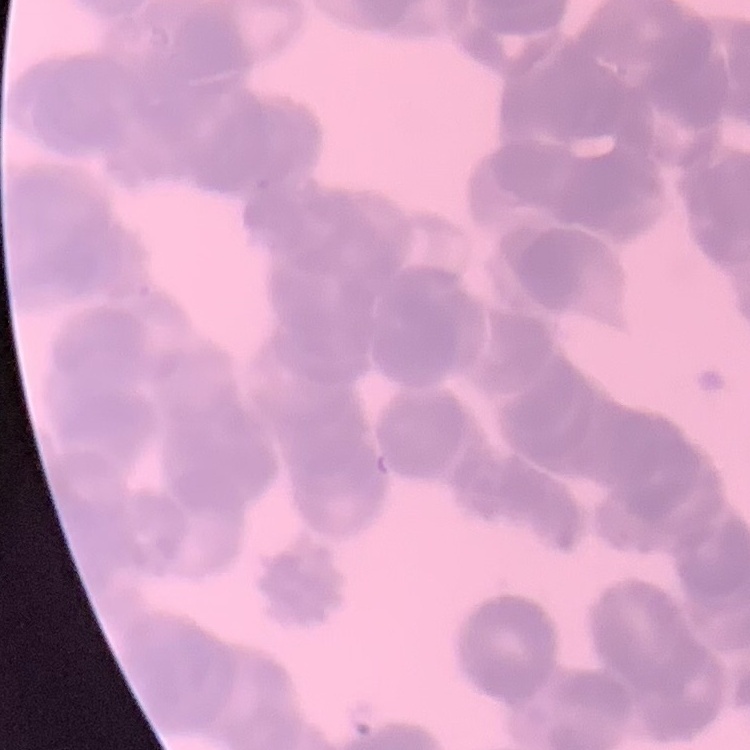

red blood cell morphology = rouleaux formation
image type = square crop of a larger photomicrograph
stain = Field's or Giemsa
preparation = thin blood film